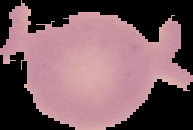
preparation = thin blood film
malaria status = uninfected
image size = 193×130 pixels
image type = cell region segmented out of the field of view; surrounding area masked to black